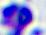

Summary:
  - Modality: micrograph
  - Identification: leukocyte
  - Magnification: 400x